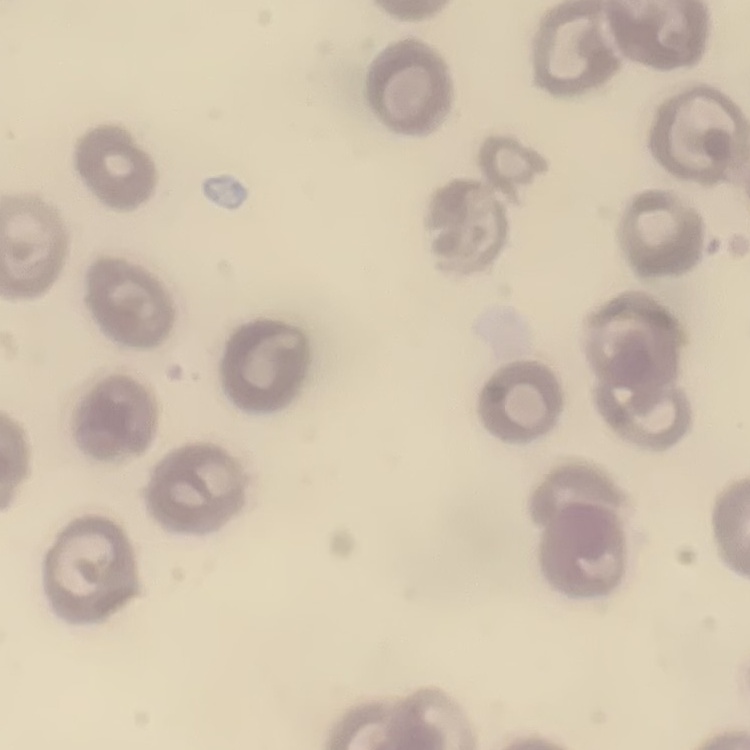

Summary:
  - Red blood cell morphology: no rouleaux formation
  - Image type: square crop of a larger photomicrograph
  - Preparation: thin peripheral smear
  - Stain: Field's or Giemsa